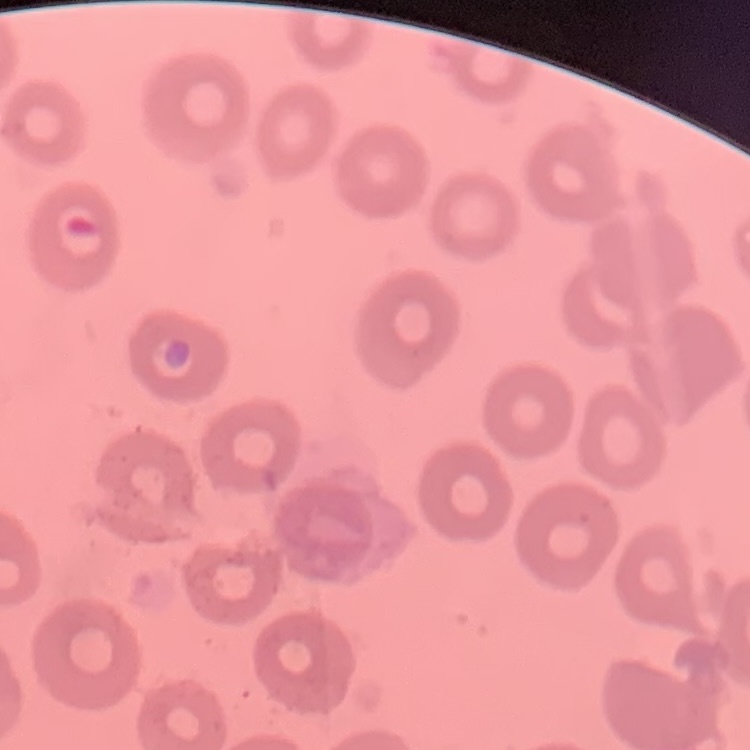
red blood cell morphology = no rouleaux formation
stain = Field's or Giemsa
preparation = thin peripheral smear
image type = square crop of a larger photomicrograph